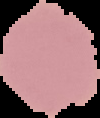

Summary:
  - Image size: 100×118 pixels
  - Image type: segmented cell region with the area outside set to black
  - Preparation: thin blood film
  - Malaria status: uninfected